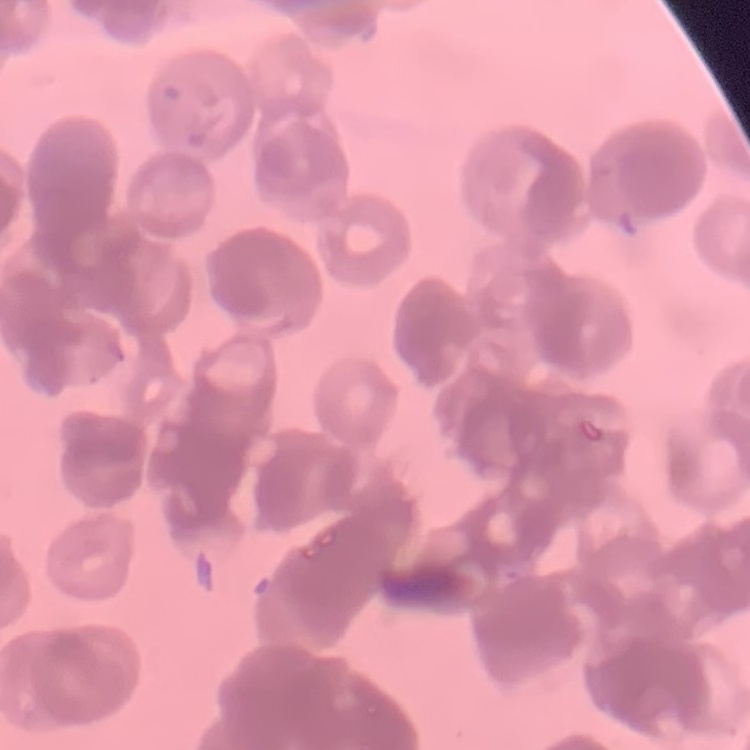 The red blood cells exhibit rouleaux formation. Thin blood film. Stained with either Field's or Giemsa. Square crop of a larger photomicrograph.